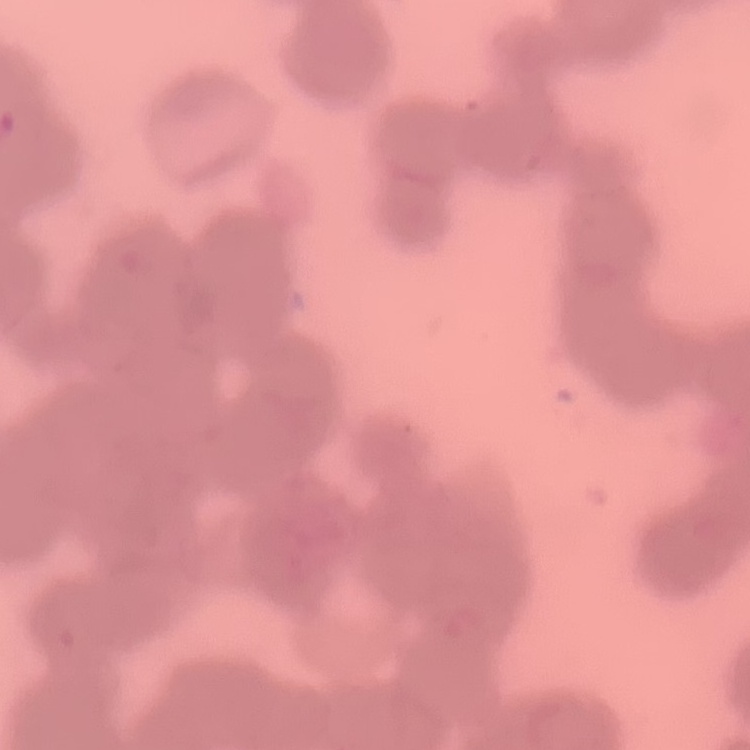
red_blood_cell_morphology: rouleaux formation
stain: Field's or Giemsa
image_type: square crop of a larger photomicrograph
preparation: thin peripheral smear